Classify this cell by malaria status.
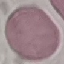
It is uninfected.

Summary:
  - Capture: smartphone camera at the microscope eyepiece
  - Preparation: thin smear
  - Stain: Giemsa
  - Image type: automatically extracted cell patch, resized to 64 × 64 pixels